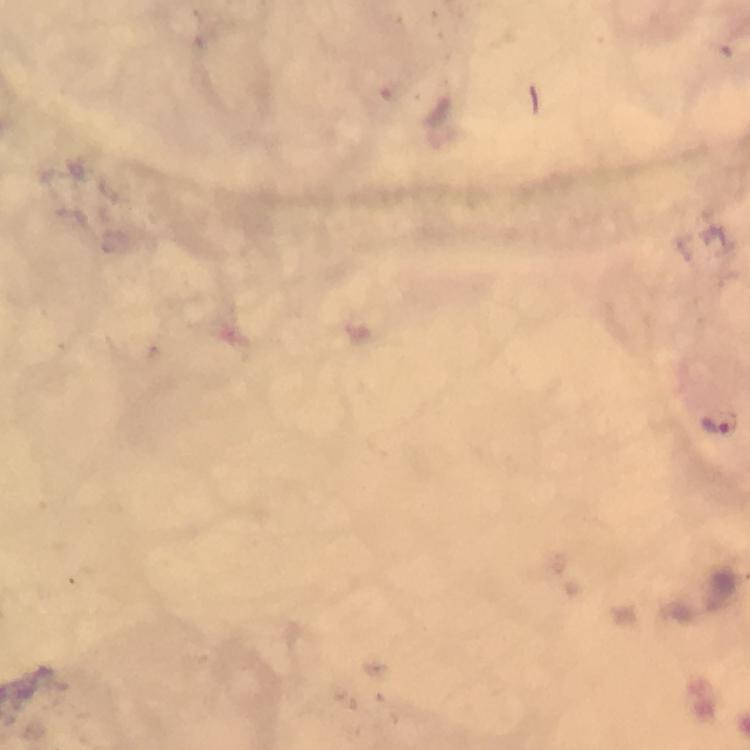

{
  "image_size": "750×750 pixels",
  "cropped_from": "one field of view",
  "context": "from a diagnostic examination for malaria",
  "stain": "Giemsa",
  "preparation": "thick blood smear",
  "malaria_parasite_locations": "approximate centers as (x, y) in pixels: (713, 426)",
  "immersion_oil": "applied",
  "capture": "smartphone mounted on the microscope",
  "magnification": "100x"
}